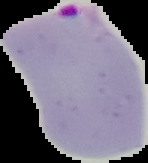 Malaria status: parasitized. From a thin blood smear. Image is 148×163 pixels. Cell region segmented out of the field of view; the surrounding area is masked to black.